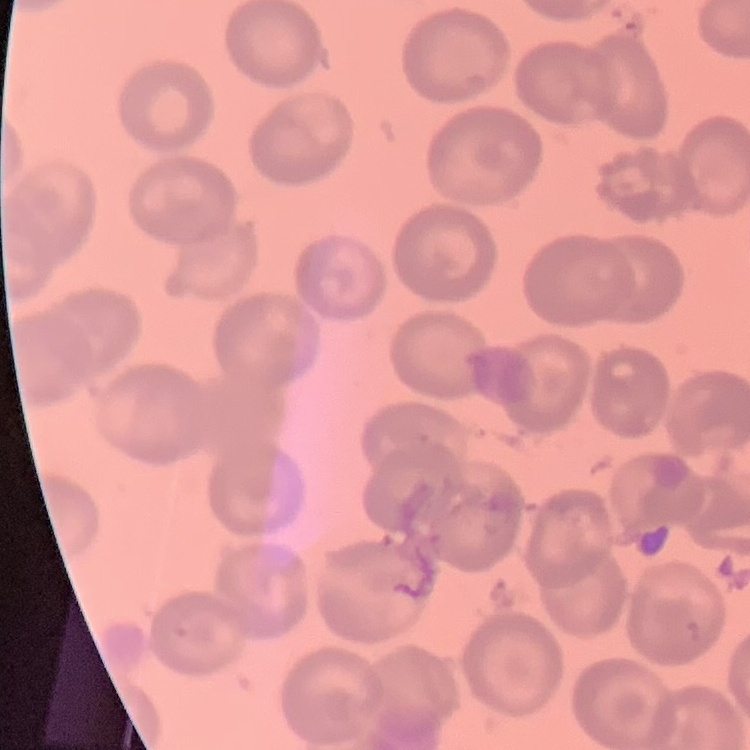

{
  "erythrocyte_morphology": "no rouleaux formation",
  "stain": "Field's or Giemsa",
  "preparation": "thin blood film",
  "image_type": "square crop of a larger photomicrograph"
}